Identify the parasite.
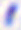

Toxoplasma gondii.

modality = photomicrograph
magnification = 400x